Assess this cell for malaria.
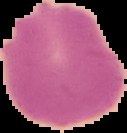

It is uninfected.

Summary:
  - Image size: 127×133 pixels
  - Image type: segmented cell region with the area outside set to black
  - Preparation: thin blood smear